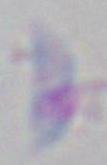
Summary:
  - Modality: micrograph
  - Identification: Toxoplasma gondii
  - Magnification: 1000x